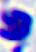
Summary:
  - Identification: leukocyte
  - Modality: micrograph
  - Magnification: 400x